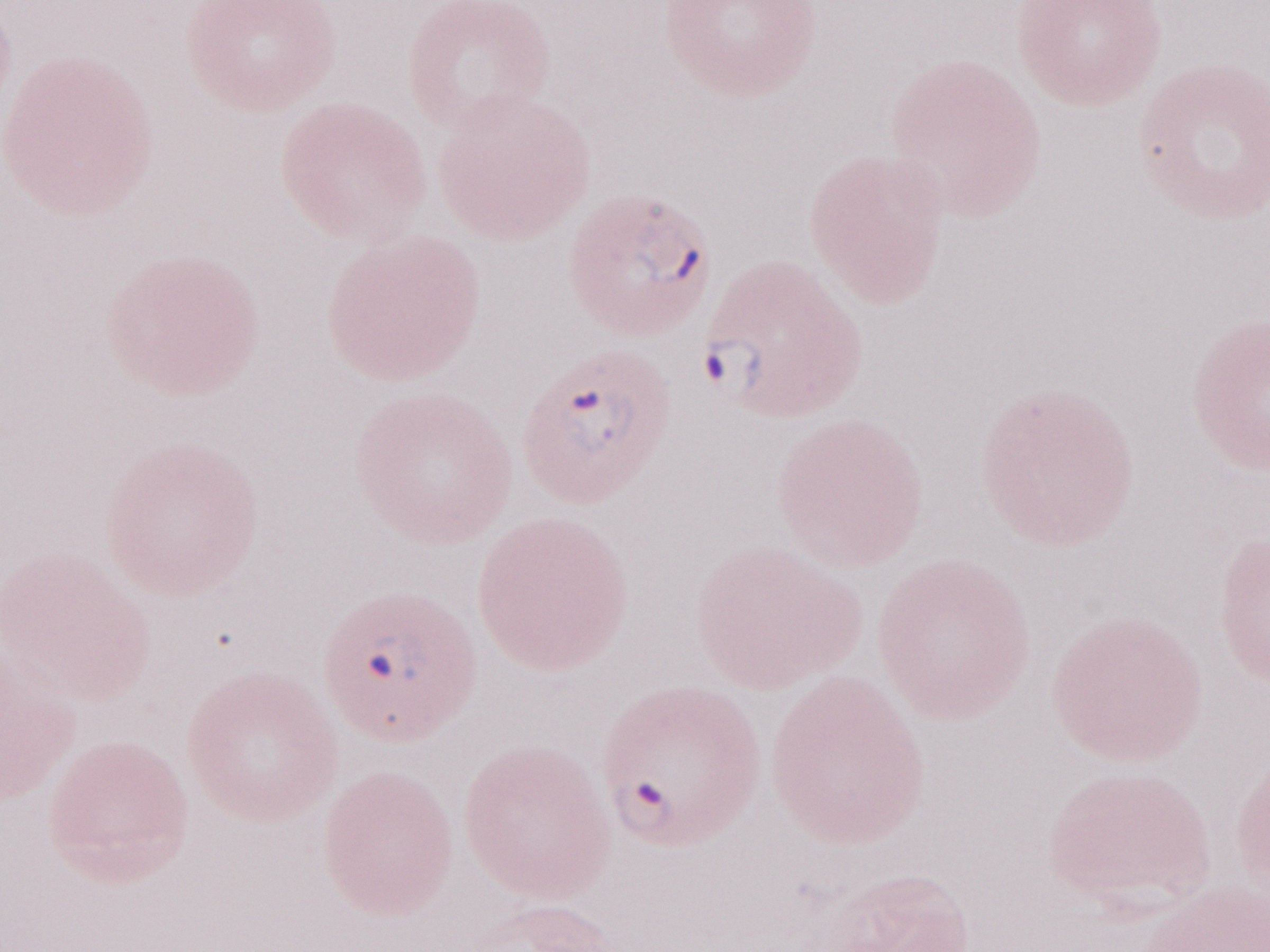 Olympus BX43 microscope, Olympus DP73 camera. May-Grünwald-Giemsa (MGG) stain. 1,000x magnification. Patient diagnosis: malaria infection. Single field of view. Thin blood smear. Image is 1270×952 pixels.